Locate every Plasmodium parasite.
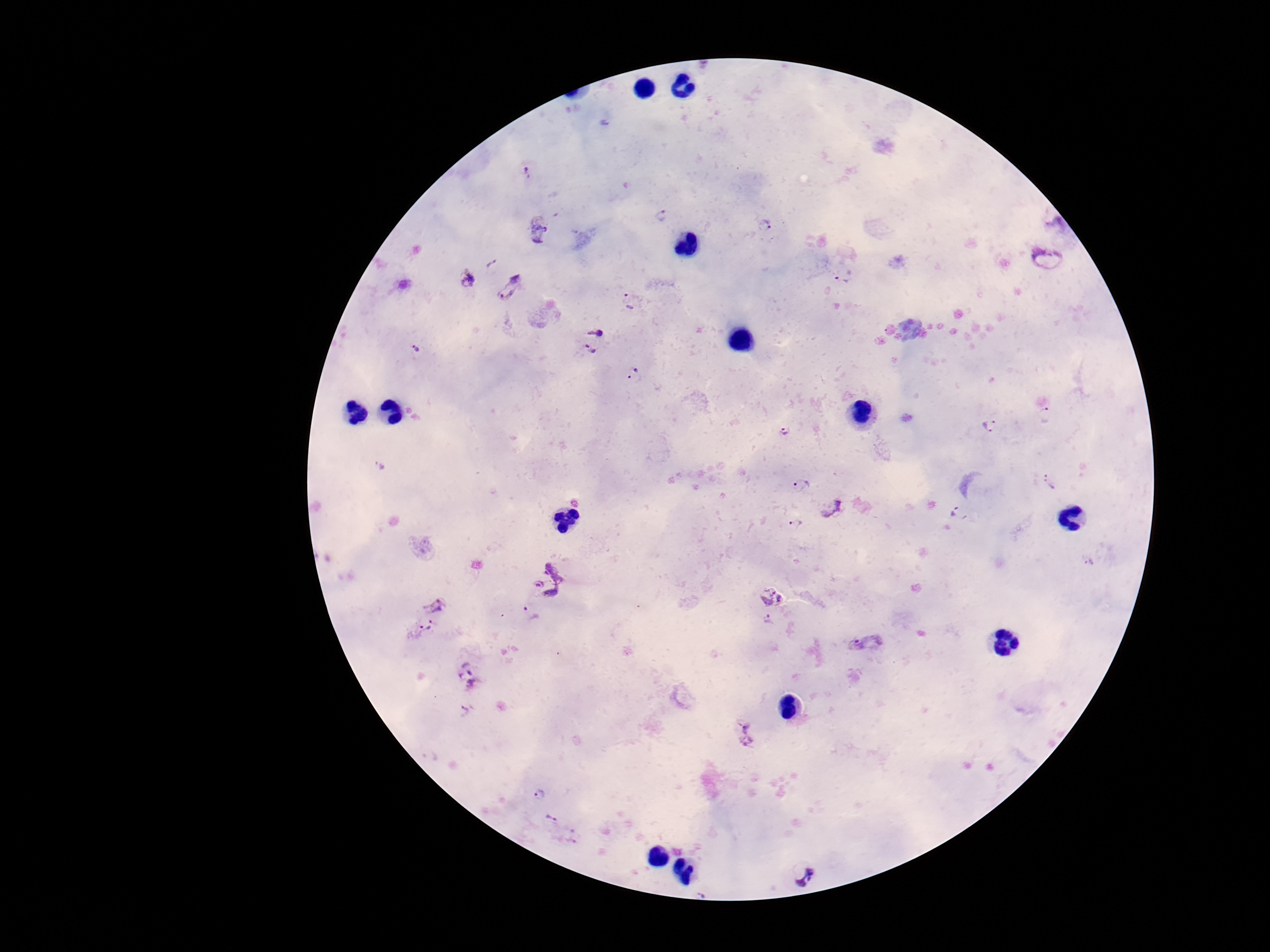
Approximate centers as (x, y) in pixels.
Plasmodium parasites: (528, 173), (662, 217), (764, 225), (539, 232), (1045, 258), (493, 263), (843, 276), (468, 279), (512, 288), (631, 300), (598, 330), (415, 349), (588, 354), (635, 376), (1046, 415), (990, 425), (786, 431), (379, 465), (1052, 483), (801, 487), (834, 507), (959, 513), (797, 525), (1089, 562), (561, 565), (541, 596), (773, 596), (437, 604), (769, 624), (422, 630), (866, 643), (469, 679), (465, 711), (744, 733), (541, 795), (552, 818), (803, 872), (702, 889).

Summary:
  - Capture: smartphone camera through the microscope eyepiece
  - Preparation: thick peripheral-blood smear
  - Field of view: one from this slide
  - Patient malaria status: infected
  - Stain: Giemsa
  - Magnification: 100x
  - Image size: 1270×952 pixels